Assess this cell for malaria.
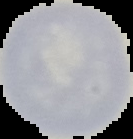

It is uninfected.

Image is 133×139 pixels. From a thin blood smear. Cell region segmented out of the field of view; the surrounding area is masked to black.